Classify this cell by malaria status.
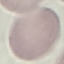

Uninfected.

Summary:
  - Stain: Giemsa
  - Capture: smartphone camera at the microscope eyepiece
  - Preparation: thin blood film
  - Image type: cell patch, automatically extracted from a larger field of view and resized to 64 × 64 pixels